Outline each blood parasite and name the species.
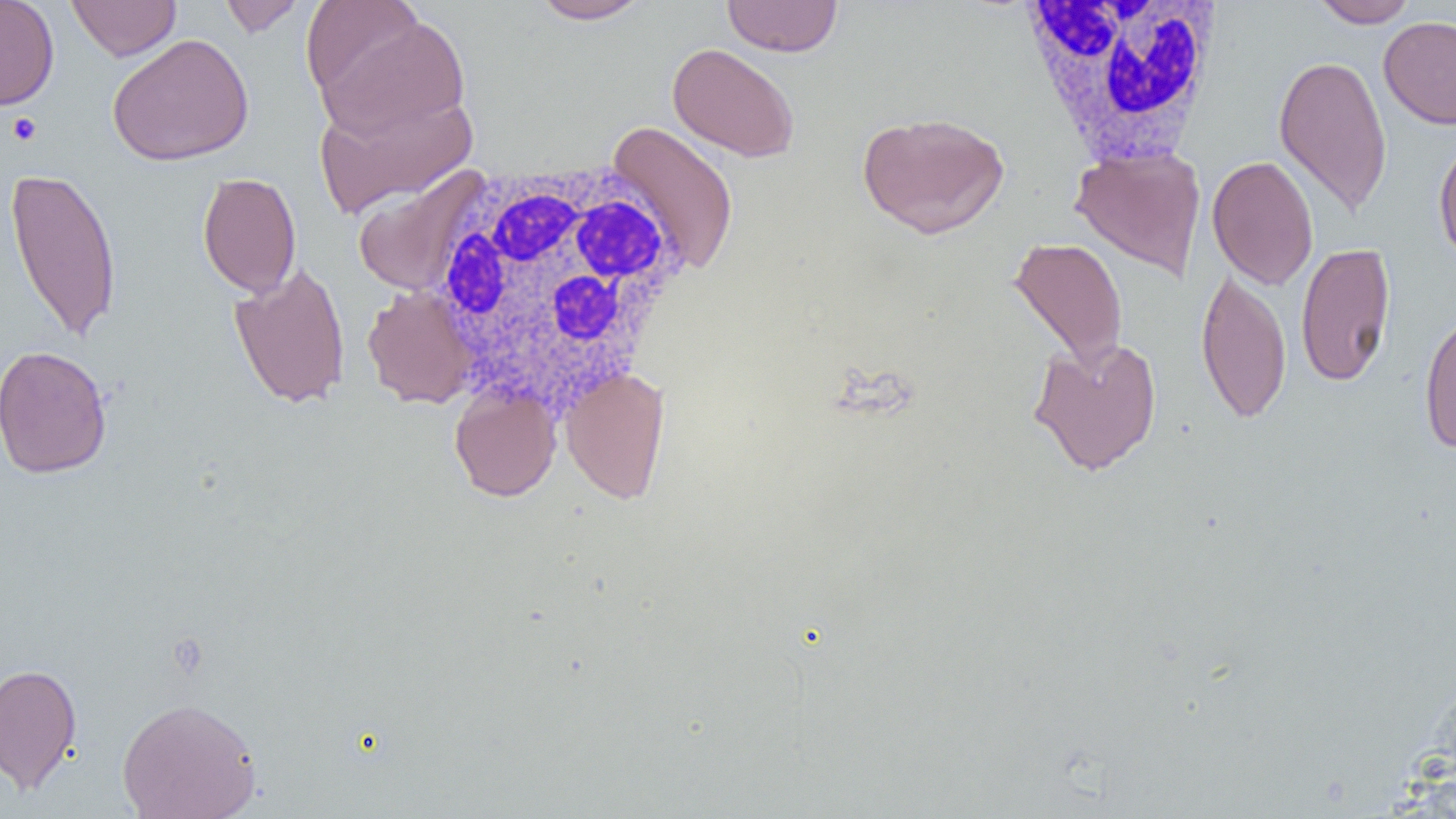

No blood parasites observed.

Summary:
  - Coordinate format: approximate bounding boxes as (x1, y1, x2, y2) in pixels
  - Platelet locations: (6, 112, 43, 146)
  - White blood cell locations: (1015, 1, 1231, 168), (422, 160, 690, 415)
  - Uninfected red blood cell locations: (0, 0, 59, 110), (68, 0, 180, 61), (219, 0, 307, 37), (527, 0, 654, 24), (722, 0, 843, 57), (1310, 0, 1419, 28), (310, 10, 472, 143), (1379, 16, 1456, 130), (107, 32, 254, 166), (667, 43, 800, 162), (1273, 53, 1393, 216), (313, 90, 477, 218), (857, 111, 1009, 239), (605, 120, 741, 276), (1433, 133, 1456, 264), (1070, 146, 1206, 281), (1207, 154, 1319, 290), (5, 164, 123, 342), (351, 169, 489, 297), (197, 171, 301, 298), (1007, 236, 1129, 374), (1295, 242, 1396, 387), (228, 262, 351, 409), (1196, 265, 1292, 425), (362, 285, 477, 409), (1418, 306, 1456, 454), (1027, 336, 1163, 476), (0, 345, 113, 479), (561, 368, 670, 504), (449, 385, 561, 501), (0, 662, 82, 794), (117, 696, 262, 819)
  - Slide-level diagnosis: negative for blood parasites
  - Image size: 1456×819 pixels
  - Modality: light microscopy
  - Field of view: one of a larger specimen
  - Magnification: 1000x
  - Preparation: thin blood smear